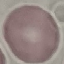
Malaria status: uninfected. Giemsa-stained preparation. Automatically extracted cell patch, resized to 64 × 64 pixels. Acquired by smartphone through the microscope eyepiece. Thin blood film.